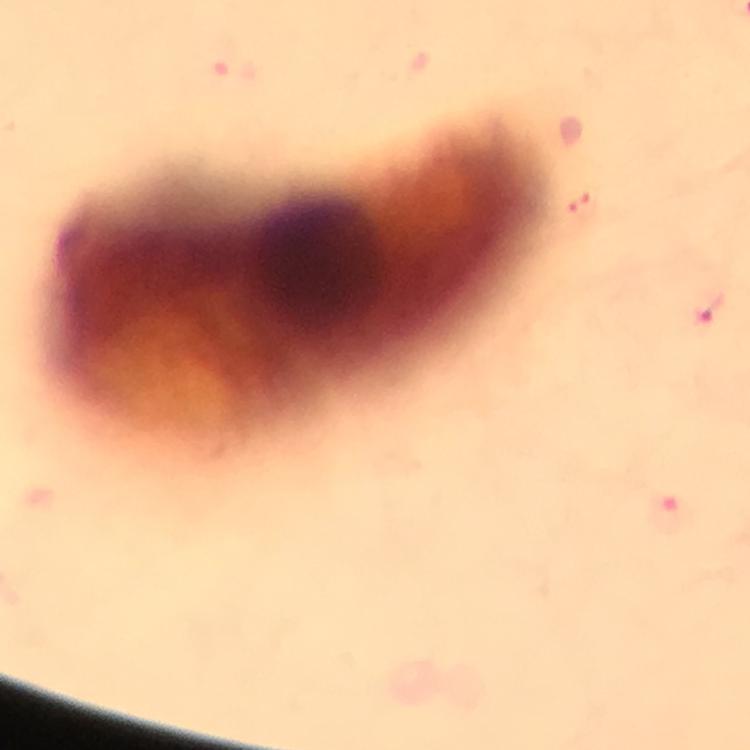
capture = smartphone photograph through a microscope
Plasmodium parasite locations = approximate centers as (x, y) in pixels: (584, 203), (708, 307), (673, 512)
cropped from = one field of view
context = from a diagnostic examination for malaria
image size = 750×750 pixels
magnification = 100x
immersion oil = applied
preparation = thick smear
stain = Giemsa